Mark where leukocytes are.
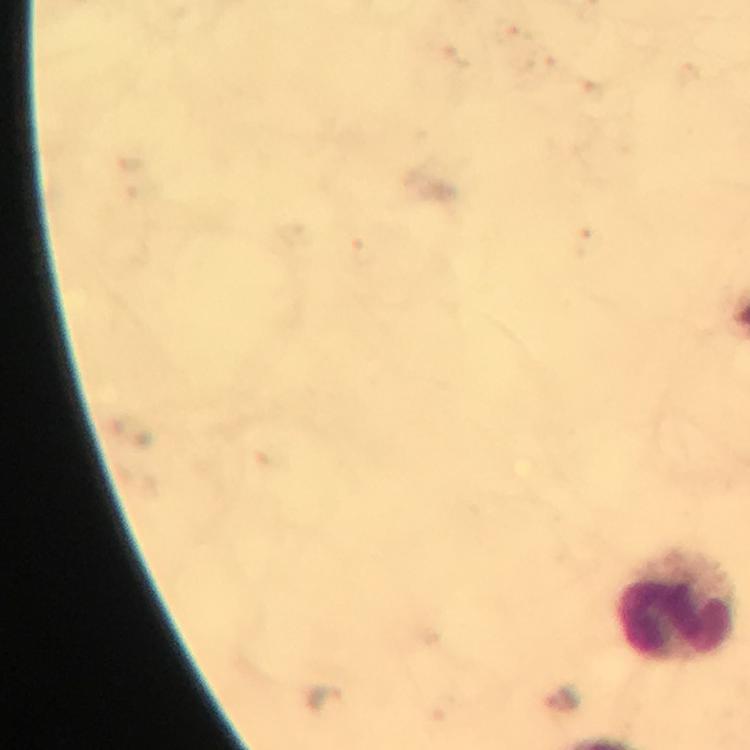
Approximate centers as [x, y] in pixels.
Leukocytes: [678, 606].

image size = 750×750 pixels
magnification = 100x
cropped from = a single field of view
immersion oil = applied
context = from a malaria diagnostic workup
preparation = thick blood smear
capture = smartphone photograph through a microscope
malaria parasites = none seen
stain = Giemsa